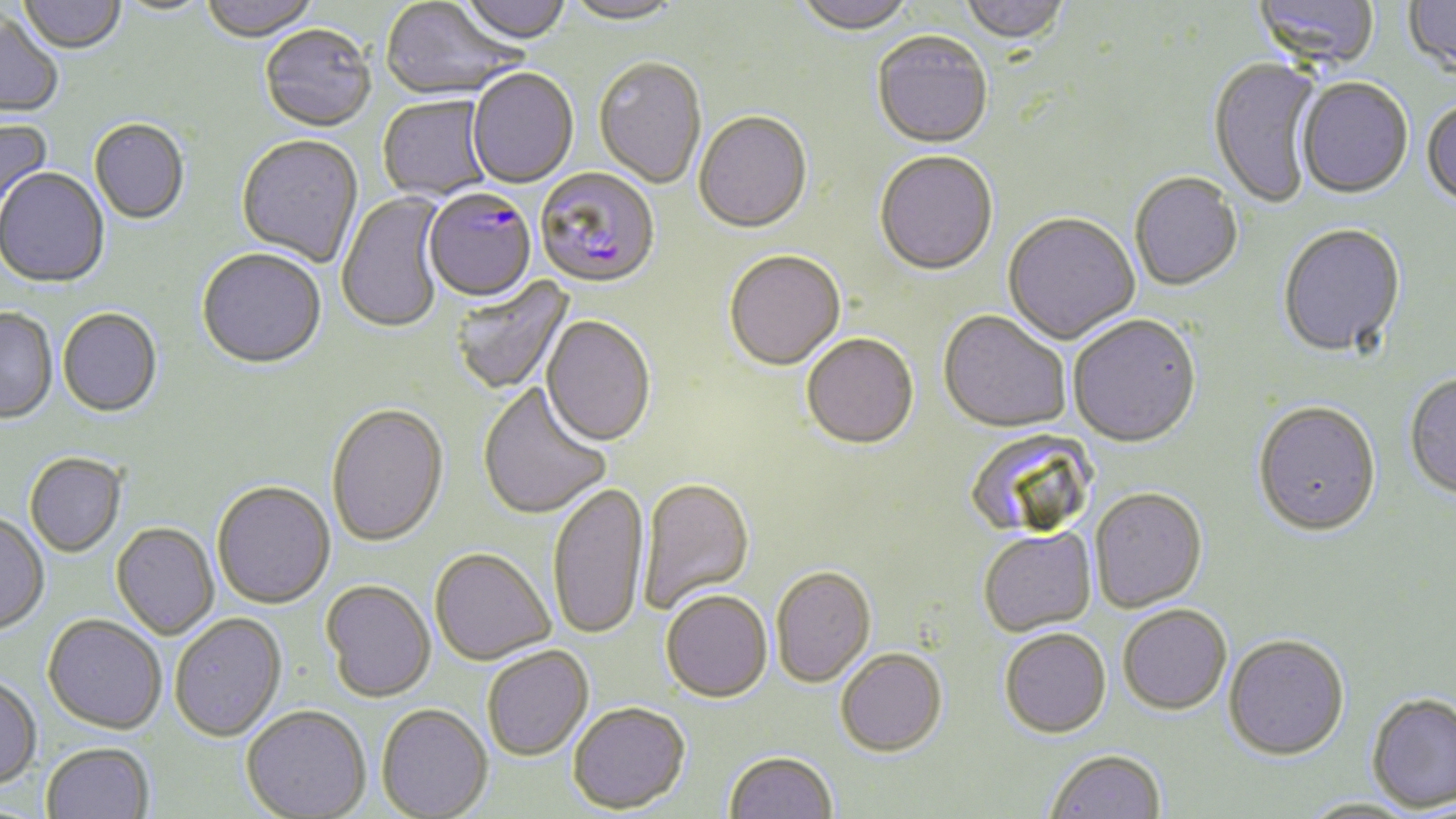
slide-level diagnosis = Plasmodium falciparum
stain = May-Grünwald-Giemsa
image size = 1456×819 pixels
Plasmodium falciparum-infected red blood cell locations = approximate bounding boxes as (x1,y1)-(x2,y2) corner pairs in pixels: (534,169)-(660,292), (423,192)-(536,304)
modality = light microscopy
uninfected red blood cell locations = approximate bounding boxes as (x1,y1)-(x2,y2) corner pairs in pixels: (17,0)-(125,56), (198,0)-(320,44), (380,0)-(526,103), (458,0)-(571,47), (561,0)-(684,28), (793,0)-(917,38), (958,0)-(1071,48), (1252,0)-(1379,72), (1402,0)-(1456,81), (112,1)-(215,20), (0,14)-(63,120), (260,27)-(376,135), (871,34)-(993,151), (1208,56)-(1323,210), (594,59)-(707,191), (466,70)-(579,190), (1296,80)-(1413,201), (378,96)-(492,201), (1422,100)-(1456,212), (694,113)-(812,236), (0,117)-(53,227), (89,120)-(190,226), (236,136)-(364,268), (874,153)-(998,278), (0,168)-(110,290), (1129,174)-(1243,293), (337,191)-(448,336), (1002,214)-(1140,347), (1277,225)-(1407,361), (196,250)-(327,372), (724,253)-(846,374), (453,273)-(577,395), (0,310)-(57,425), (58,310)-(163,419), (938,312)-(1071,436), (1069,316)-(1202,450), (540,317)-(656,449), (802,336)-(919,453), (1404,375)-(1456,503), (477,383)-(613,522), (1252,404)-(1382,540), (326,405)-(450,550), (966,427)-(1097,541), (24,454)-(128,558), (638,479)-(755,613), (212,483)-(335,610), (548,483)-(650,642), (1090,489)-(1208,613), (0,513)-(49,635), (111,524)-(219,641), (978,529)-(1096,637), (430,550)-(555,667), (771,569)-(876,689), (320,581)-(436,703), (661,593)-(773,705), (1117,605)-(1231,716), (169,614)-(287,743), (42,615)-(167,735), (999,629)-(1112,739), (1223,636)-(1350,762), (482,646)-(594,762), (835,651)-(948,759), (0,676)-(42,790), (1367,694)-(1456,813), (568,703)-(691,814), (376,704)-(493,819), (241,706)-(371,818), (41,742)-(154,819), (1044,749)-(1167,819), (724,752)-(838,819), (1297,798)-(1419,818)
preparation = thin blood smear
field of view = single
magnification = 1000x